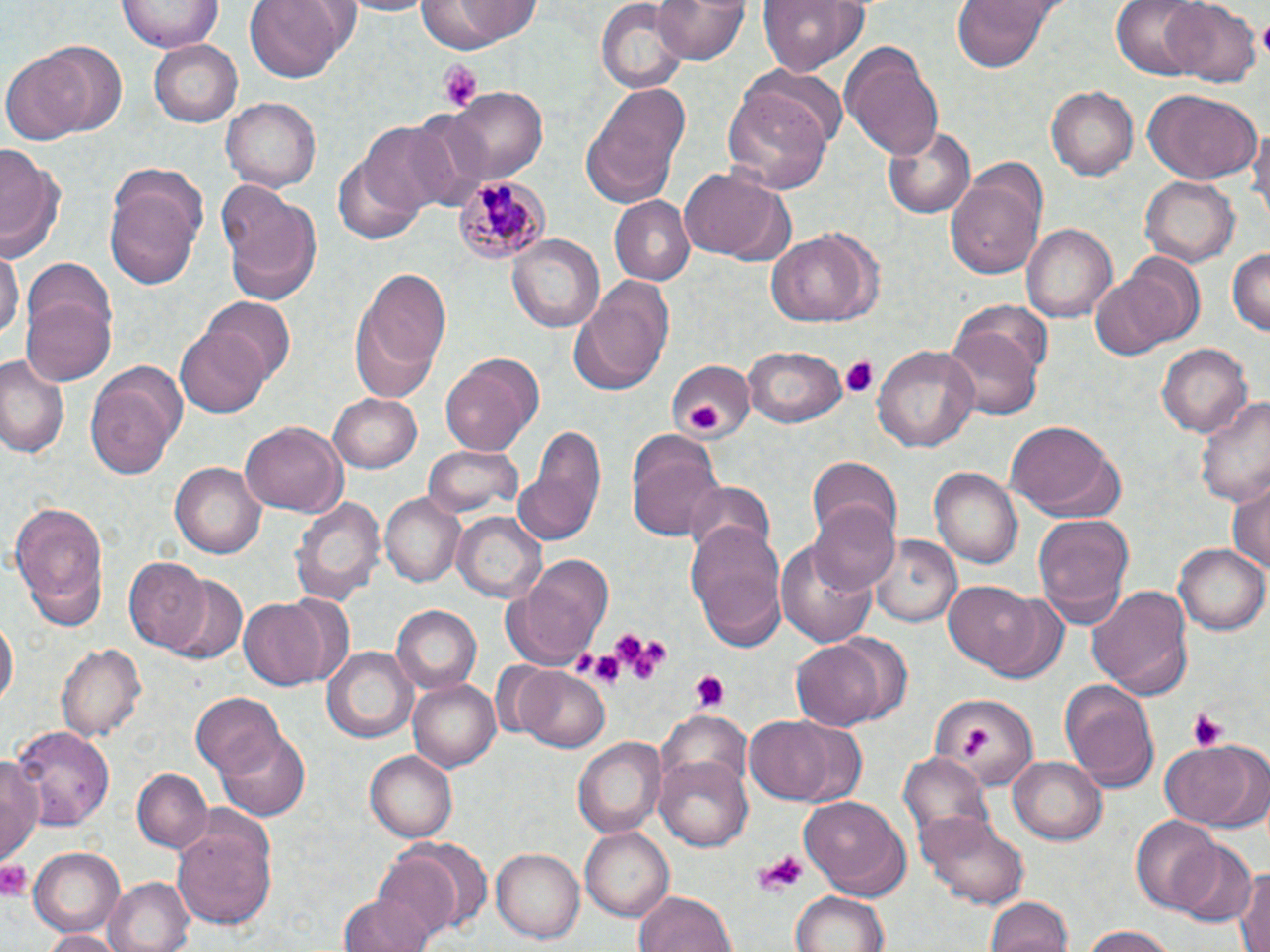

{
  "slide_level_diagnosis": "Plasmodium malariae",
  "magnification": "1000x",
  "preparation": "thin blood film",
  "field_of_view": "single",
  "platelet_locations": "approximate bounding boxes as [x1, y1, x2, y2] in pixels: [1256, 16, 1270, 60], [439, 63, 481, 112], [842, 356, 878, 399], [687, 401, 727, 433], [610, 630, 671, 683], [587, 647, 630, 687], [687, 672, 728, 713], [1186, 708, 1230, 750], [955, 730, 996, 755], [754, 850, 804, 898], [0, 857, 36, 900]",
  "plasmodium_malariae_infected_red_blood_cell_locations": "approximate bounding boxes as [x1, y1, x2, y2] in pixels: [454, 172, 552, 266]",
  "image_size": "1270×952 pixels",
  "modality": "light microscopy",
  "stain": "May-Grünwald-Giemsa",
  "uninfected_red_blood_cell_locations": "approximate bounding boxes as [x1, y1, x2, y2] in pixels: [119, 0, 222, 53], [125, 0, 235, 104], [245, 0, 359, 81], [337, 0, 438, 16], [416, 0, 538, 55], [655, 0, 753, 66], [755, 0, 874, 73], [953, 0, 1054, 74], [1113, 0, 1212, 79], [1164, 1, 1259, 86], [596, 3, 688, 91], [25, 40, 125, 137], [149, 40, 241, 126], [841, 42, 945, 160], [2, 55, 93, 147], [736, 63, 850, 148], [580, 81, 693, 207], [1047, 84, 1139, 181], [447, 86, 546, 184], [721, 88, 832, 193], [1141, 89, 1260, 184], [223, 98, 321, 190], [409, 109, 493, 206], [1248, 118, 1270, 225], [357, 121, 461, 218], [880, 125, 976, 219], [0, 145, 66, 266], [332, 156, 424, 243], [947, 164, 1047, 280], [677, 166, 789, 264], [103, 177, 205, 291], [1139, 177, 1240, 267], [218, 183, 324, 303], [610, 197, 695, 284], [1022, 223, 1116, 323], [766, 229, 881, 328], [507, 234, 605, 333], [1227, 248, 1269, 338], [0, 250, 21, 346], [1122, 253, 1208, 346], [349, 264, 452, 400], [19, 268, 116, 387], [1089, 269, 1187, 362], [570, 277, 676, 392], [203, 298, 295, 386], [954, 299, 1054, 385], [176, 324, 274, 417], [944, 326, 1040, 421], [873, 343, 980, 452], [1156, 343, 1252, 438], [745, 346, 848, 430], [440, 350, 544, 456], [0, 353, 72, 459], [85, 360, 187, 481], [663, 360, 753, 440], [328, 391, 424, 472], [1196, 393, 1270, 509], [518, 420, 606, 544], [238, 421, 348, 519], [1003, 423, 1126, 521], [627, 428, 725, 543], [422, 446, 521, 519], [807, 455, 902, 544], [169, 461, 266, 557], [930, 467, 1023, 572], [682, 479, 775, 559], [1228, 481, 1269, 583], [380, 493, 465, 588], [290, 494, 385, 606], [7, 500, 112, 628], [808, 502, 901, 596], [453, 511, 546, 601], [1033, 511, 1134, 625], [685, 520, 787, 648], [868, 535, 963, 629], [775, 538, 882, 648], [1174, 541, 1269, 636], [505, 555, 614, 668], [123, 558, 213, 654], [168, 577, 248, 665], [941, 582, 1059, 678], [1087, 584, 1195, 698], [239, 594, 336, 690], [390, 604, 481, 693], [1, 617, 17, 715], [790, 639, 888, 731], [57, 642, 146, 746], [323, 646, 417, 743], [513, 666, 612, 754], [407, 679, 499, 771], [1060, 682, 1160, 787], [191, 692, 284, 777], [929, 694, 1037, 790], [657, 711, 753, 800], [744, 714, 862, 805], [14, 724, 114, 829], [211, 725, 310, 822], [575, 735, 667, 837], [1160, 738, 1264, 830], [366, 749, 459, 843], [0, 750, 44, 865], [898, 752, 992, 852], [656, 756, 753, 852], [1008, 756, 1106, 845], [133, 767, 211, 853], [798, 795, 911, 899], [173, 808, 278, 931], [919, 816, 1027, 906], [1130, 818, 1226, 913], [580, 825, 675, 918], [1168, 841, 1258, 927], [374, 844, 476, 943], [493, 847, 587, 941], [28, 849, 124, 938], [1234, 865, 1270, 952], [104, 876, 193, 952], [634, 889, 737, 952], [790, 890, 891, 952], [340, 893, 434, 952], [986, 896, 1072, 952], [1078, 925, 1176, 952], [39, 930, 123, 951]"
}